Report the malaria status of this cell.
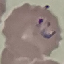
It is parasitized.

Summary:
  - Capture: smartphone camera at the microscope eyepiece
  - Stain: Giemsa
  - Image type: cell patch, automatically extracted from a larger field of view and resized to 64 × 64 pixels
  - Preparation: thin blood smear